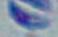

Summary:
  - Identification: Toxoplasma gondii
  - Modality: micrograph
  - Magnification: 1000x